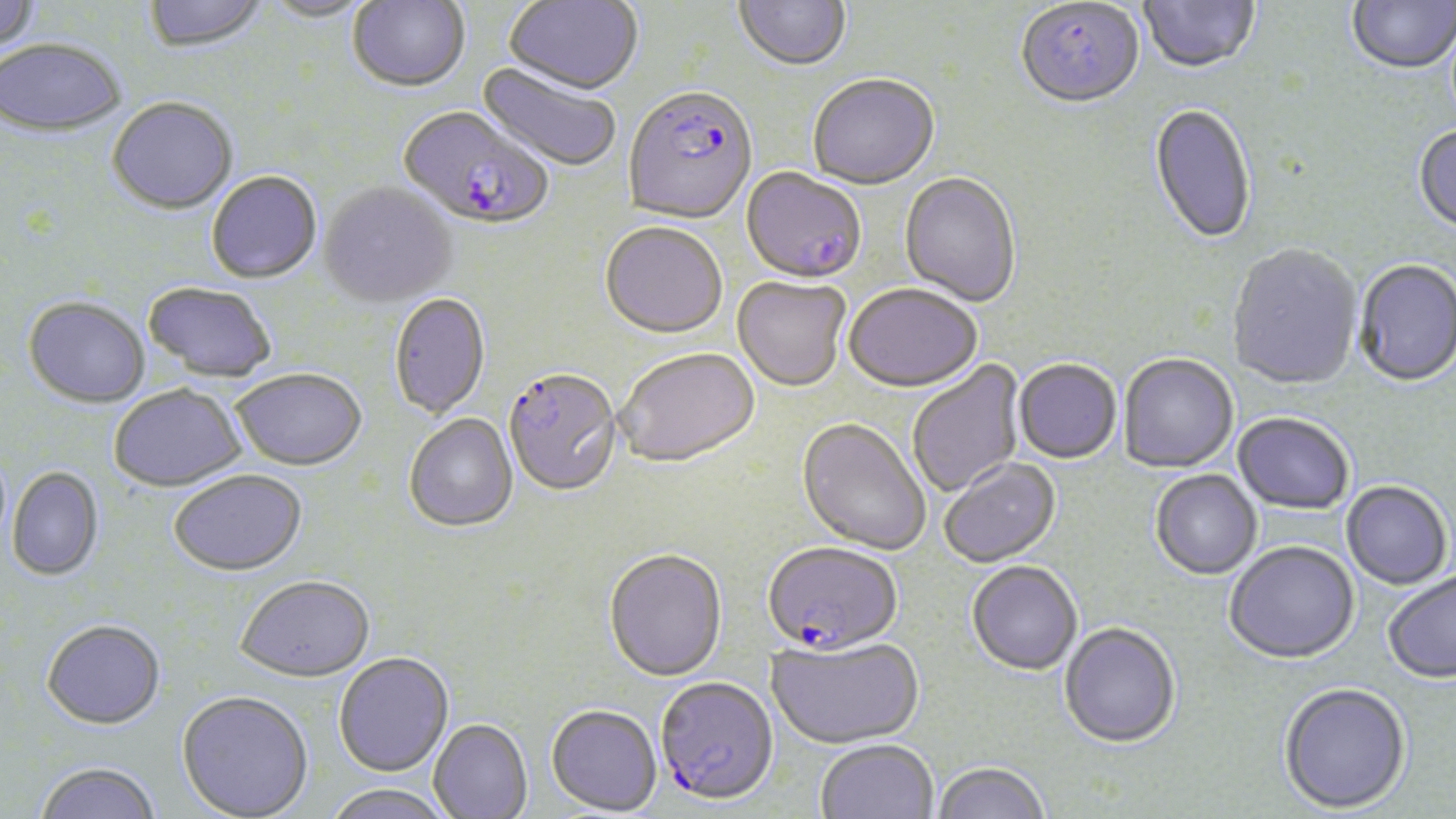

Approximate bounding boxes as [x1, y1, x2, y2] in pixels. Plasmodium falciparum-infected red blood cell locations: [1016, 2, 1144, 112], [623, 87, 758, 228], [397, 107, 554, 234], [742, 169, 866, 285], [504, 370, 624, 499], [762, 541, 902, 656], [655, 676, 778, 804]. Uninfected red blood cell locations: [0, 0, 41, 54], [142, 0, 270, 55], [348, 0, 470, 93], [504, 0, 643, 97], [734, 0, 851, 74], [1139, 0, 1260, 76], [1347, 0, 1456, 76], [257, 1, 377, 24], [0, 40, 126, 139], [476, 62, 622, 174], [808, 76, 940, 192], [107, 98, 238, 216], [1149, 104, 1256, 248], [1413, 126, 1456, 236], [206, 172, 322, 285], [899, 173, 1021, 308], [319, 183, 458, 310], [599, 223, 727, 341], [1227, 245, 1362, 392], [1354, 261, 1456, 389], [732, 277, 851, 393], [142, 282, 277, 384], [844, 286, 982, 396], [389, 294, 491, 420], [23, 298, 150, 410], [615, 349, 760, 471], [1118, 355, 1239, 474], [906, 359, 1026, 499], [1013, 360, 1122, 465], [230, 370, 367, 473], [109, 386, 247, 493], [405, 414, 518, 533], [1232, 414, 1354, 516], [796, 419, 931, 556], [938, 458, 1062, 568], [6, 468, 104, 581], [168, 471, 308, 578], [1150, 471, 1262, 581], [1342, 482, 1452, 591], [1224, 543, 1360, 666], [603, 548, 727, 682], [967, 562, 1082, 675], [1383, 571, 1456, 687], [236, 577, 375, 685], [41, 620, 166, 731], [1059, 623, 1181, 748], [766, 635, 924, 748], [334, 653, 454, 777], [1278, 685, 1412, 815], [176, 691, 314, 819], [546, 704, 662, 815], [429, 719, 533, 819], [814, 738, 939, 819], [931, 760, 1050, 819], [33, 762, 161, 819], [321, 783, 456, 819]. Slide-level diagnosis: Plasmodium falciparum. Light microscopy. 1000x magnification. Thin blood film. Image is 1456×819 pixels. Single field of view. May-Grünwald-Giemsa-stained preparation.